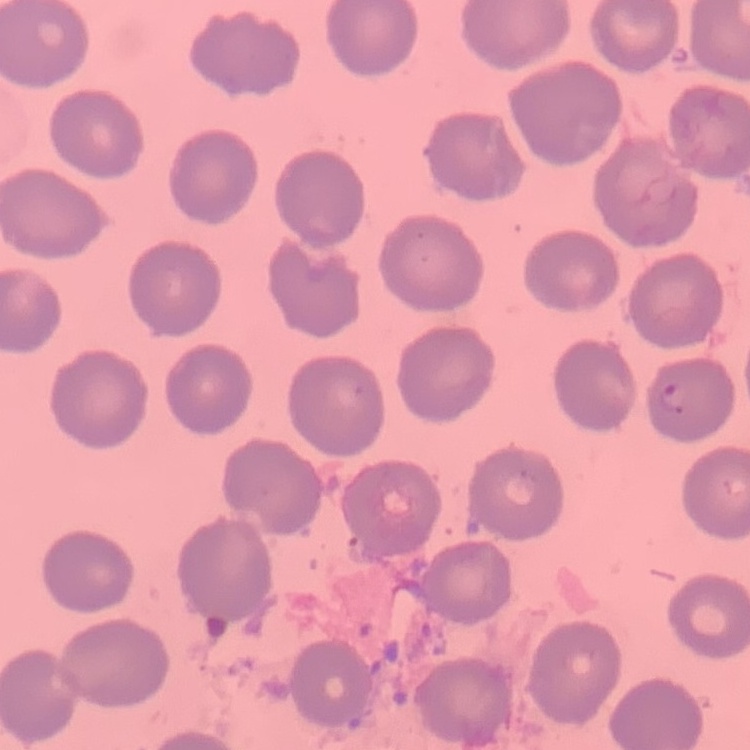

The red blood cells exhibit no rouleaux formation. Stained with either Field's or Giemsa. Square crop of a larger photomicrograph. Thin blood smear.